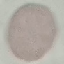
{
  "malaria_status": "uninfected",
  "preparation": "thin blood smear",
  "stain": "Giemsa",
  "image_type": "automatically extracted cell patch, resized to 64 × 64 pixels",
  "capture": "smartphone through the microscope eyepiece"
}